Assess this cell for malaria.
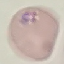
Parasitized.

Giemsa-stained preparation. Thin blood film. Acquired by smartphone through the microscope eyepiece. Automatically extracted cell patch, resized to 64 × 64 pixels.